Give the position of every Plasmodium parasite visible.
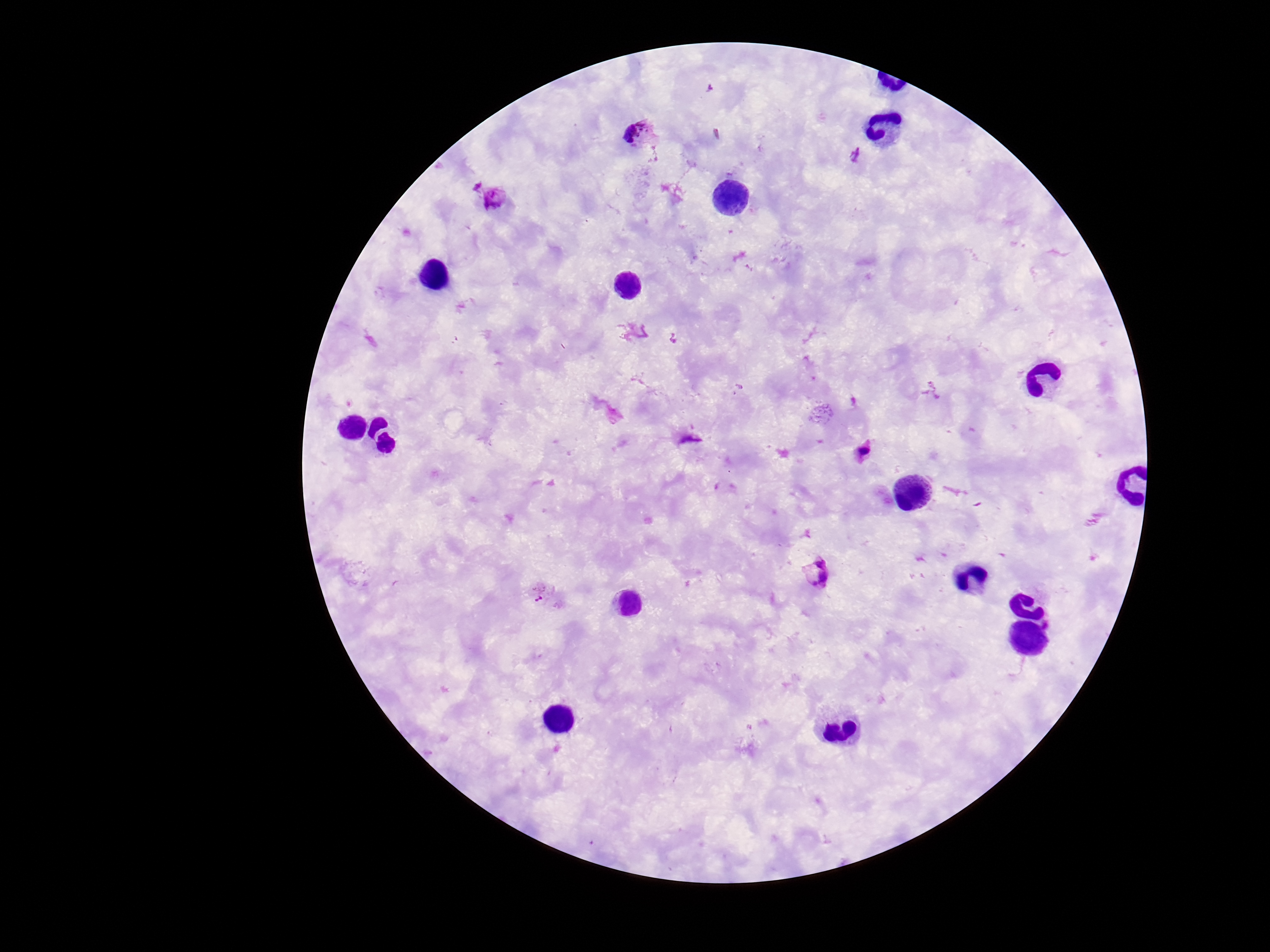
Approximate centers as (x, y) in pixels.
Plasmodium parasites: (641, 133), (856, 156), (494, 198), (863, 451), (817, 574), (544, 595).

Summary:
  - Image size: 1270×952 pixels
  - Magnification: 100x
  - Capture: smartphone camera through the microscope eyepiece
  - Stain: Giemsa
  - Preparation: thick blood film
  - Field of view: single
  - Patient malaria status: positive